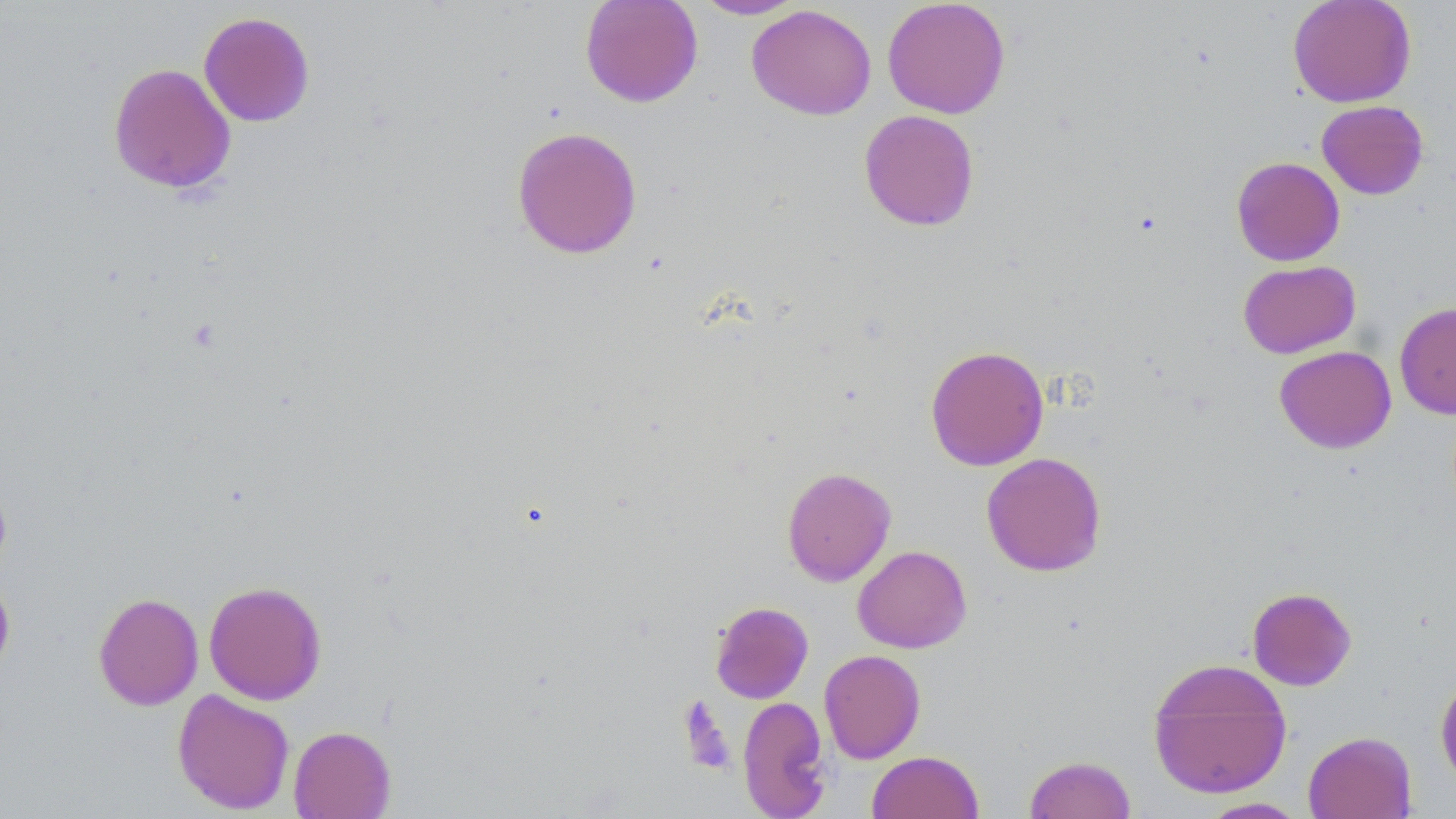 Approximate bounding boxes as named x1/y1/x2/y2 corners in pixels. Uninfected red blood cell locations: (x1=579, y1=0, x2=704, y2=108), (x1=693, y1=0, x2=807, y2=20), (x1=882, y1=0, x2=1011, y2=119), (x1=1287, y1=0, x2=1417, y2=108), (x1=746, y1=4, x2=877, y2=120), (x1=198, y1=11, x2=315, y2=127), (x1=108, y1=62, x2=236, y2=195), (x1=1317, y1=100, x2=1429, y2=199), (x1=858, y1=109, x2=980, y2=231), (x1=511, y1=126, x2=642, y2=259), (x1=1231, y1=157, x2=1345, y2=266), (x1=1237, y1=260, x2=1361, y2=359), (x1=1394, y1=301, x2=1456, y2=420), (x1=925, y1=344, x2=1049, y2=471), (x1=1274, y1=345, x2=1397, y2=453), (x1=981, y1=452, x2=1107, y2=576), (x1=781, y1=466, x2=897, y2=586), (x1=0, y1=476, x2=12, y2=581), (x1=852, y1=545, x2=972, y2=653), (x1=0, y1=573, x2=15, y2=682), (x1=203, y1=580, x2=327, y2=705), (x1=1247, y1=587, x2=1357, y2=690), (x1=93, y1=592, x2=204, y2=710), (x1=710, y1=601, x2=813, y2=704), (x1=819, y1=649, x2=926, y2=764), (x1=1147, y1=657, x2=1292, y2=800), (x1=1434, y1=674, x2=1456, y2=788), (x1=172, y1=688, x2=295, y2=815), (x1=737, y1=695, x2=833, y2=819), (x1=288, y1=724, x2=396, y2=819), (x1=1302, y1=730, x2=1417, y2=819), (x1=867, y1=751, x2=983, y2=819), (x1=1023, y1=754, x2=1137, y2=818), (x1=1197, y1=797, x2=1310, y2=818). Slide-level diagnosis: no evidence of blood parasites. Optical microscopy. Captured at 1000x magnification. May-Grünwald-Giemsa-stained preparation. Image is 1456×819 pixels. Single field of view. Thin blood smear.